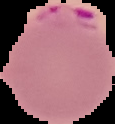
Result: Plasmodium parasites detected. From a thin blood smear. Segmented cell region on a black background. Image is 115×124 pixels.